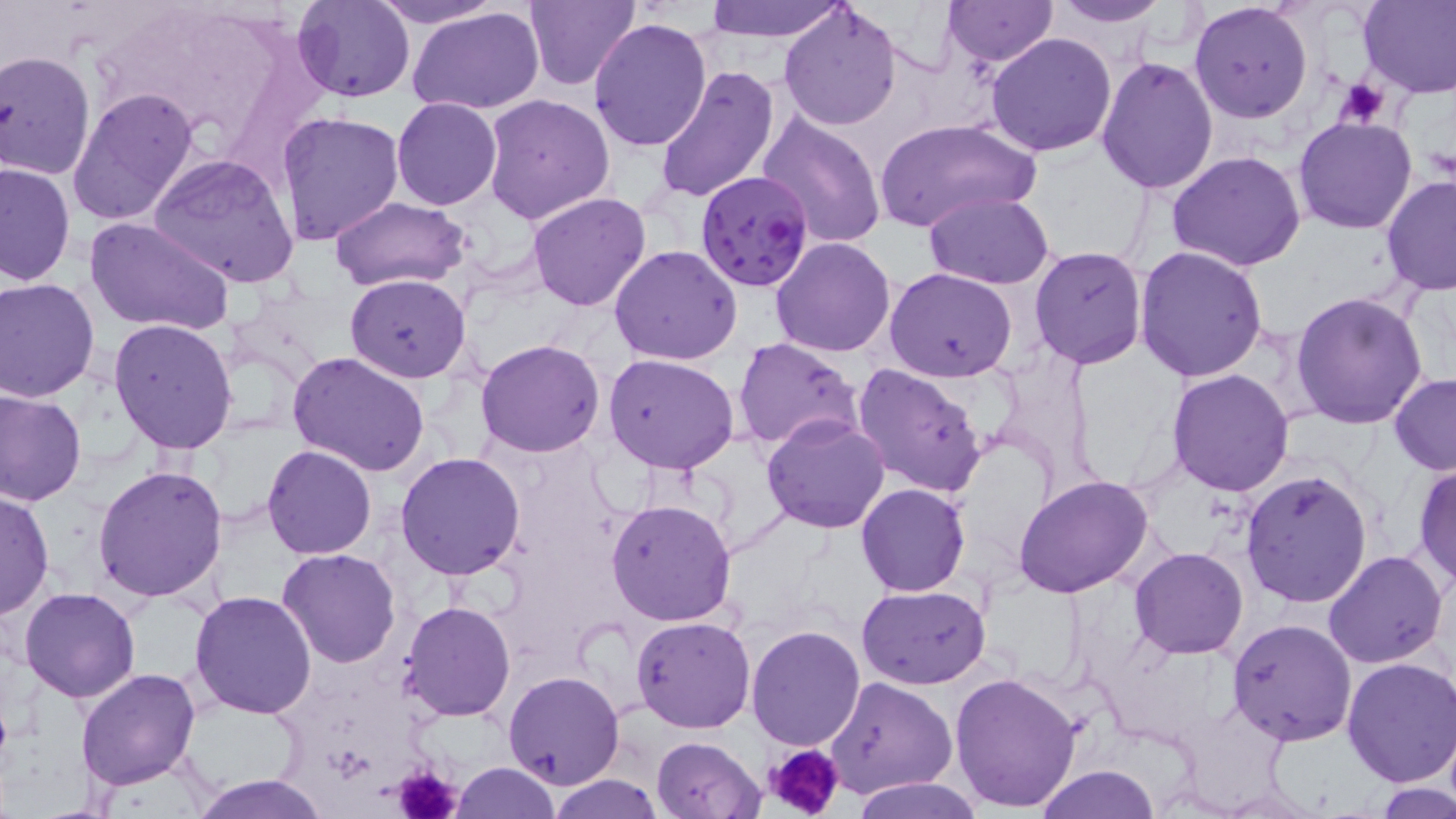

Summary:
  - Coordinate format: approximate bounding boxes as [x1, y1, x2, y2] in pixels
  - Platelet locations: [1333, 76, 1391, 125], [764, 742, 846, 819], [389, 763, 463, 819]
  - Plasmodium falciparum-infected red blood cell locations: [696, 171, 816, 295]
  - Uninfected red blood cell locations: [292, 0, 416, 102], [370, 0, 505, 28], [524, 0, 643, 92], [944, 0, 1055, 66], [702, 1, 849, 41], [777, 1, 903, 131], [1048, 1, 1170, 26], [1188, 1, 1313, 123], [1359, 1, 1456, 98], [408, 6, 546, 115], [588, 18, 713, 153], [983, 33, 1118, 156], [0, 47, 95, 179], [1096, 56, 1220, 195], [654, 65, 781, 204], [68, 85, 202, 230], [482, 93, 616, 226], [391, 97, 502, 210], [277, 112, 405, 245], [758, 112, 887, 248], [1293, 116, 1419, 236], [872, 118, 1039, 237], [1167, 151, 1306, 271], [150, 153, 302, 290], [0, 160, 75, 287], [1382, 176, 1456, 296], [923, 191, 1057, 288], [526, 192, 653, 312], [327, 196, 472, 291], [85, 217, 237, 337], [769, 236, 896, 356], [1134, 243, 1269, 382], [610, 244, 744, 365], [1030, 245, 1145, 369], [883, 267, 1018, 383], [345, 273, 472, 381], [0, 278, 100, 402], [1291, 293, 1430, 429], [109, 319, 238, 453], [733, 337, 864, 454], [475, 338, 606, 458], [287, 351, 431, 479], [603, 352, 740, 474], [850, 364, 990, 500], [1166, 370, 1296, 495], [1389, 372, 1456, 475], [0, 389, 86, 508], [761, 414, 891, 534], [262, 445, 377, 560], [395, 452, 525, 579], [1412, 461, 1456, 589], [93, 463, 228, 601], [1241, 467, 1373, 609], [1012, 475, 1154, 599], [855, 484, 969, 597], [0, 485, 54, 620], [606, 498, 738, 627], [1128, 547, 1249, 659], [277, 548, 402, 668], [1323, 549, 1449, 668], [858, 585, 989, 688], [20, 587, 140, 702], [189, 590, 318, 719], [399, 601, 516, 722], [632, 615, 755, 733], [1228, 618, 1358, 746], [745, 626, 866, 750], [1341, 655, 1456, 787], [75, 667, 200, 790], [503, 671, 625, 790], [949, 672, 1083, 813], [826, 677, 956, 799], [651, 735, 764, 818], [452, 763, 560, 818], [1034, 764, 1162, 819], [189, 772, 331, 818], [546, 775, 663, 818], [853, 776, 983, 819], [1377, 781, 1455, 818]
  - Slide-level diagnosis: Plasmodium falciparum
  - Preparation: thin blood smear
  - Image size: 1456×819 pixels
  - Stain: May-Grünwald-Giemsa
  - Field of view: single
  - Modality: light microscopy
  - Magnification: 1000x